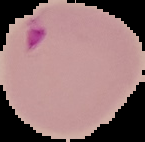
Image is 145×142 pixels. From a thin blood film. Result: malaria parasites detected. Cell region segmented out of the field of view; the surrounding area is masked to black.